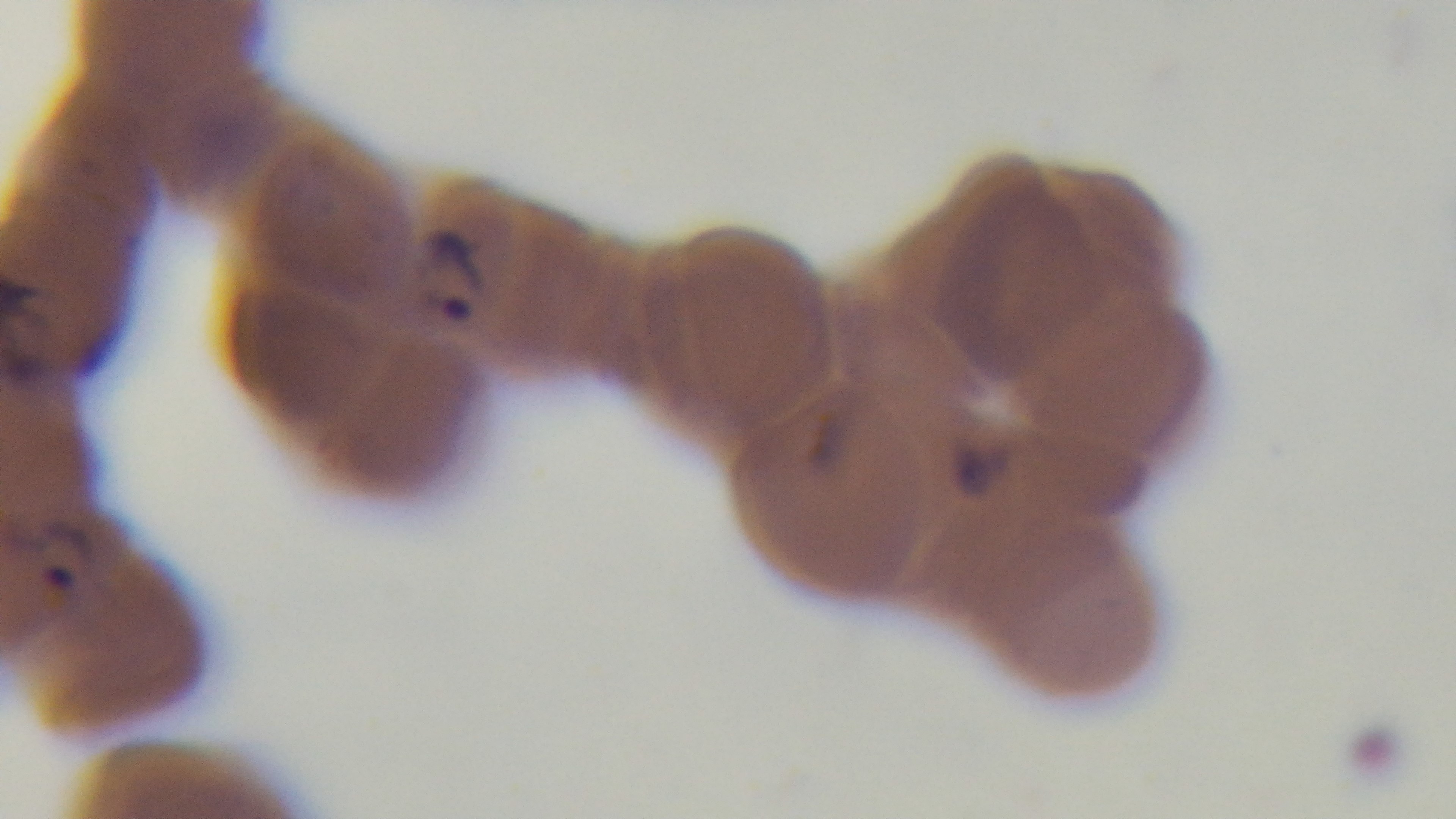
{
  "preparation": "thin smear",
  "field_of_view": "single",
  "modality": "light microscopy",
  "stain": "Giemsa",
  "malaria_status": "infected",
  "objective": "100x oil immersion",
  "capture": "mounted 4K digital camera"
}